Describe the morphology of the red blood cells.
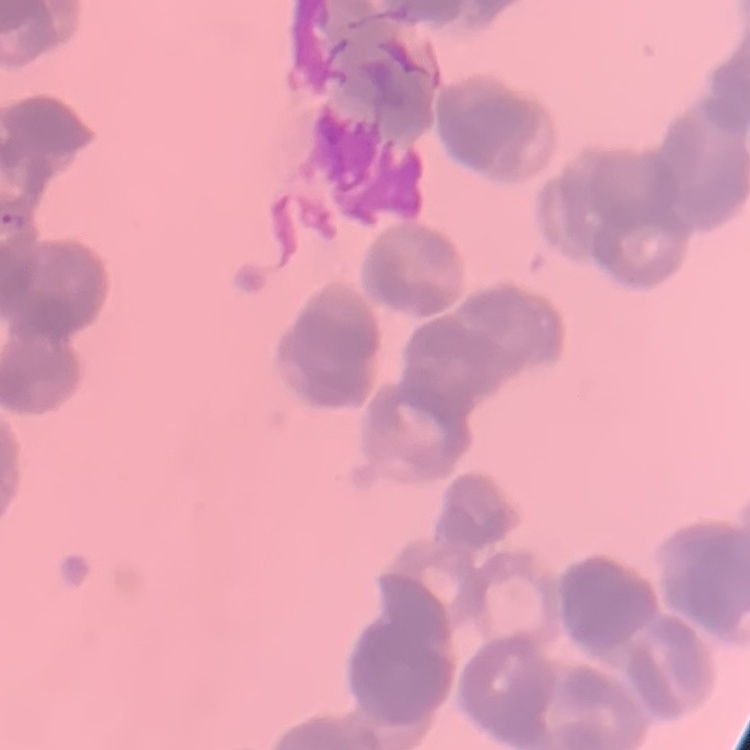

They show rouleaux formation.

{
  "stain": "Field's or Giemsa",
  "image_type": "square crop of a larger photomicrograph",
  "preparation": "thin blood smear"
}